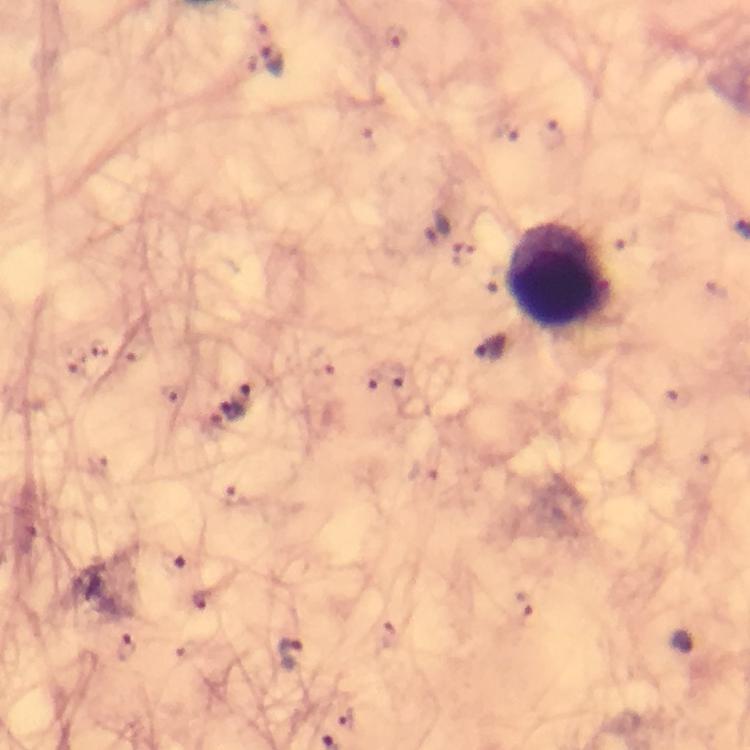
preparation: thick smear
stain: Giemsa
cropped_from: one field of view
immersion_oil: applied
malaria_parasite_locations: 'approximate centers as [x, y] in pixels: [394, 38], [271, 62], [435, 227], [463, 257], [489, 347], [75, 359], [321, 365], [397, 374], [370, 380], [242, 395], [674, 395], [229, 412], [171, 561], [200, 598], [525, 605], [128, 648], [289, 655], [348, 719]'
context: from a diagnostic examination for malaria
leukocyte_locations: 'approximate centers as [x, y] in pixels: [557, 275]'
capture: smartphone mounted on the microscope
image_size: 750×750 pixels
magnification: 100x